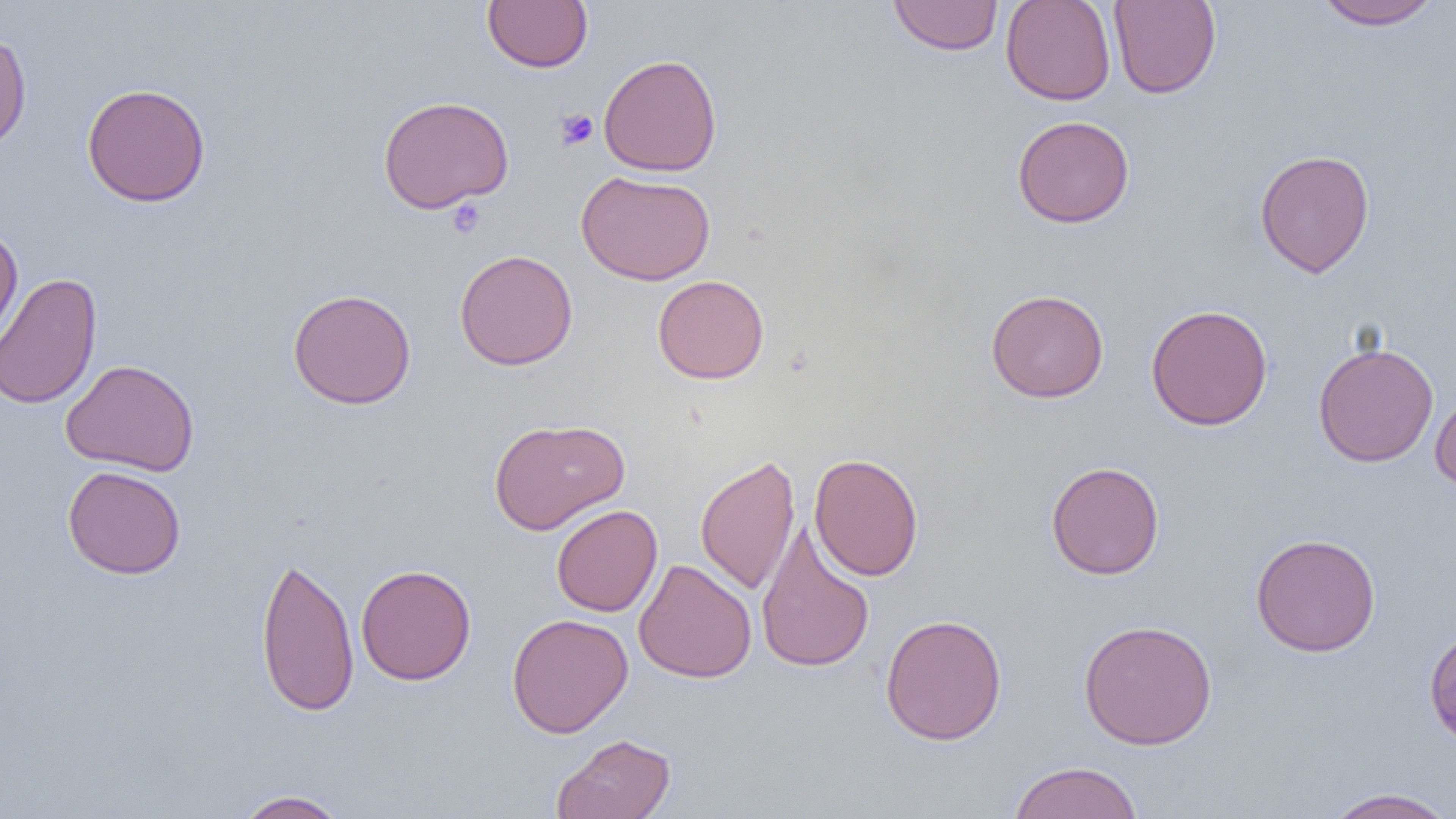

slide_level_diagnosis: negative for blood parasites
preparation: thin blood film
field_of_view: one of a larger specimen
magnification: 1000x
image_size: 1456×819 pixels
modality: optical microscopy
uninfected_red_blood_cell_locations: 'approximate bounding boxes as (x1, y1, x2, y2) in pixels: (482, 0, 593, 73), (888, 0, 1003, 56), (1000, 0, 1116, 105), (1108, 1, 1222, 99), (1311, 1, 1445, 30), (0, 32, 32, 152), (598, 53, 722, 177), (82, 82, 211, 207), (377, 95, 514, 214), (1012, 115, 1135, 228), (1254, 149, 1375, 278), (576, 170, 716, 286), (0, 224, 24, 352), (455, 249, 578, 371), (0, 272, 102, 410), (652, 274, 769, 384), (287, 288, 417, 409), (985, 289, 1109, 403), (1146, 304, 1273, 431), (1312, 341, 1439, 467), (61, 359, 200, 476), (1430, 390, 1456, 494), (489, 417, 630, 535), (809, 452, 924, 581), (695, 455, 801, 595), (1045, 461, 1165, 579), (62, 465, 186, 579), (551, 504, 663, 616), (756, 522, 875, 674), (1250, 533, 1381, 657), (255, 553, 360, 716), (633, 558, 757, 683), (356, 564, 476, 685), (506, 613, 633, 738), (879, 613, 1007, 746), (1078, 619, 1218, 749), (1423, 625, 1456, 751), (551, 733, 677, 819), (1007, 760, 1144, 819), (1322, 787, 1455, 819), (233, 789, 350, 818)'
platelet_locations: 'approximate bounding boxes as (x1, y1, x2, y2) in pixels: (555, 109, 598, 150), (446, 198, 487, 238)'